Assess this cell for malaria.
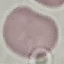

Uninfected.

Photographed with a smartphone camera at the microscope eyepiece. Thin smear of blood. Giemsa-stained preparation. Automatically extracted cell patch, resized to 64 × 64 pixels.